State the preparation type.
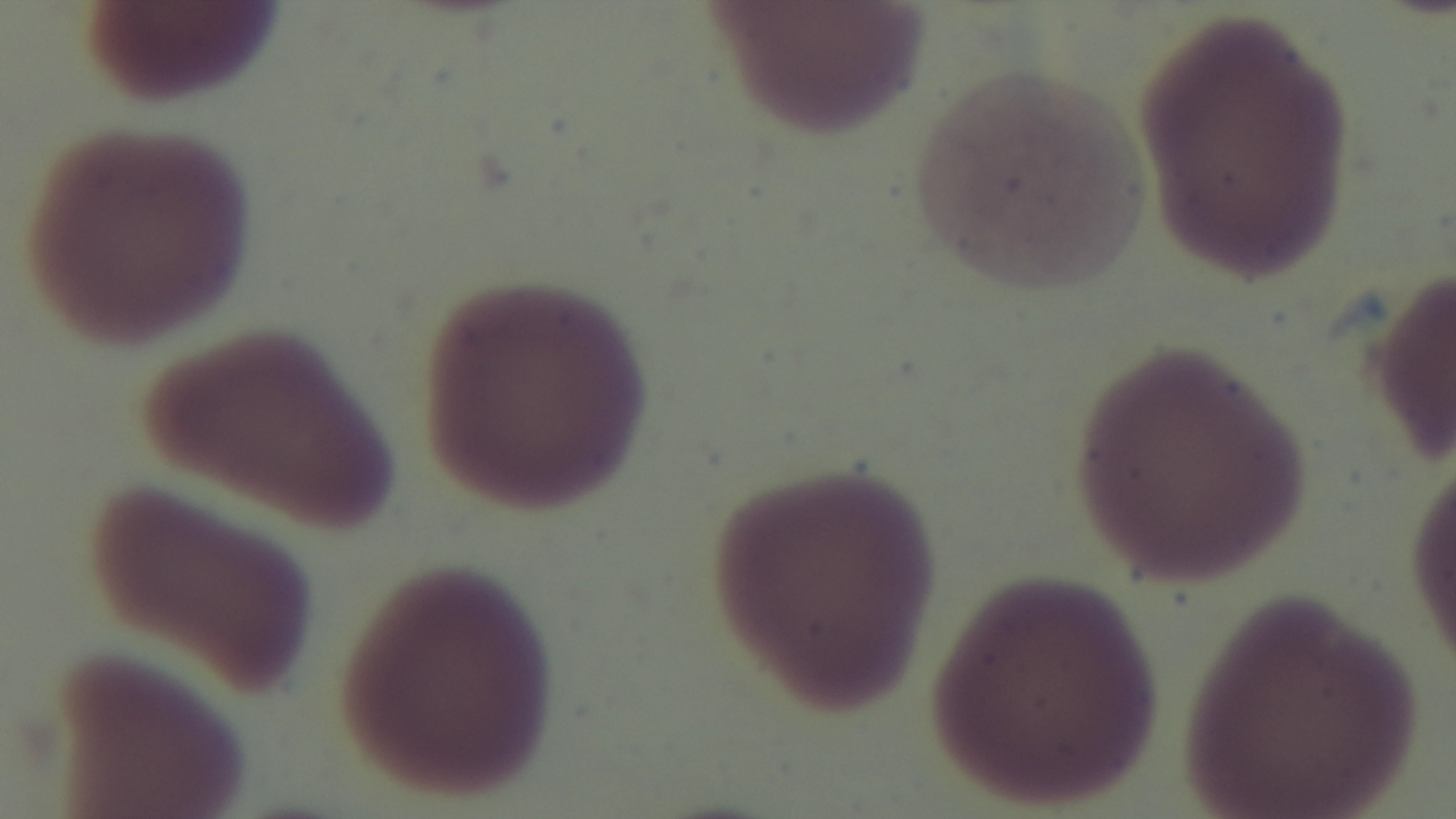
A thin smear.

Summary:
  - Objective: 100x oil immersion
  - Field of view: single
  - Malaria status: negative
  - Stain: Giemsa
  - Capture: mounted 4K digital camera
  - Modality: light microscopy